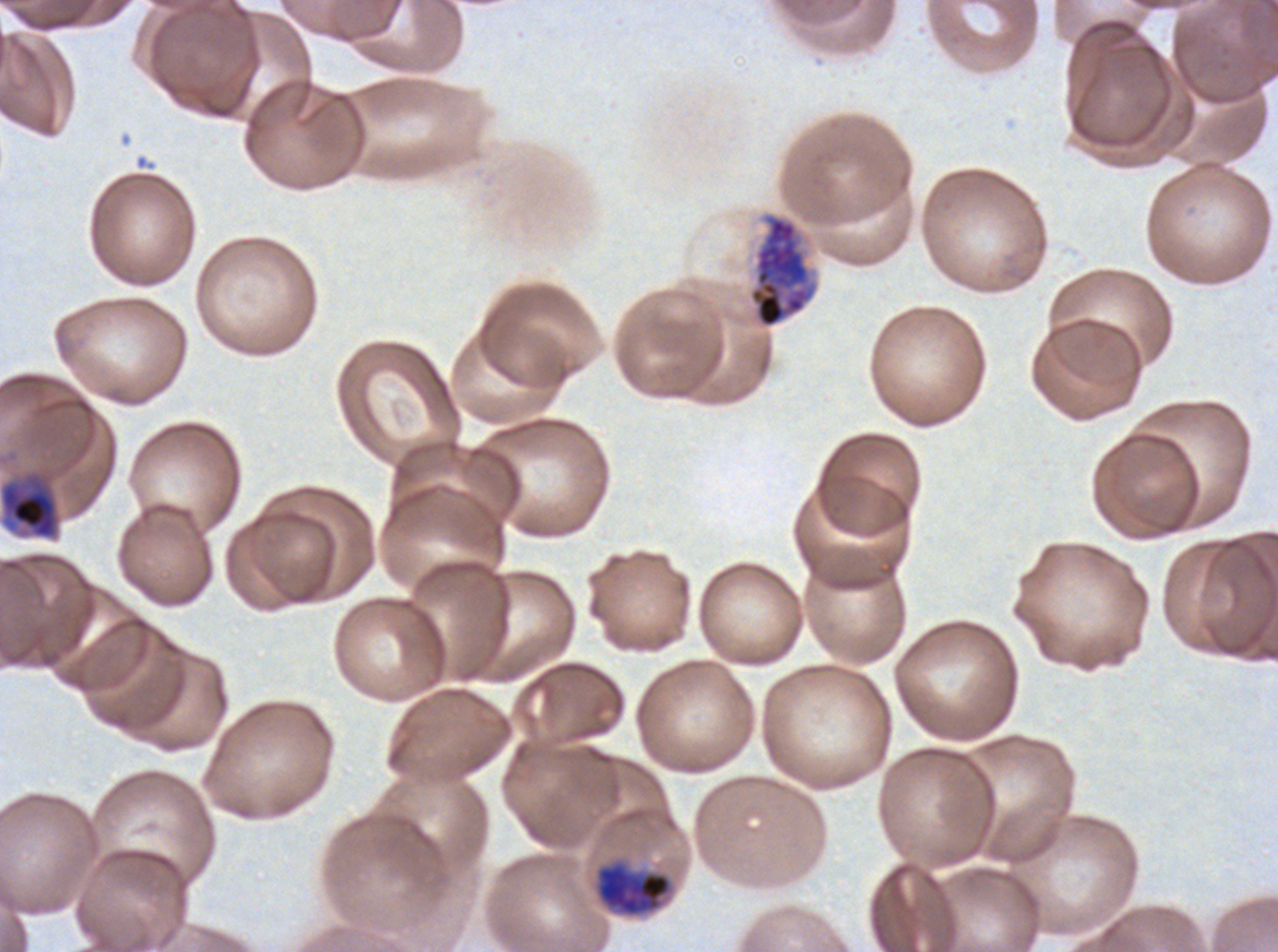
notation = approximate bounding boxes as {x1, y1, x2, y2} in pixels
early schizont locations = {749, 215, 813, 328}
late trophozoite locations = {0, 472, 60, 540}, {594, 858, 674, 918}
specimen = Plasmodium falciparum cultured ex vivo for 24 to 48 hours, from a patient in The Gambia
stain = Giemsa
preparation = thin blood film
life-cycle stages observed = late trophozoite, early schizont
field of view = one sub-image of a larger composite
image size = 1278×952 pixels